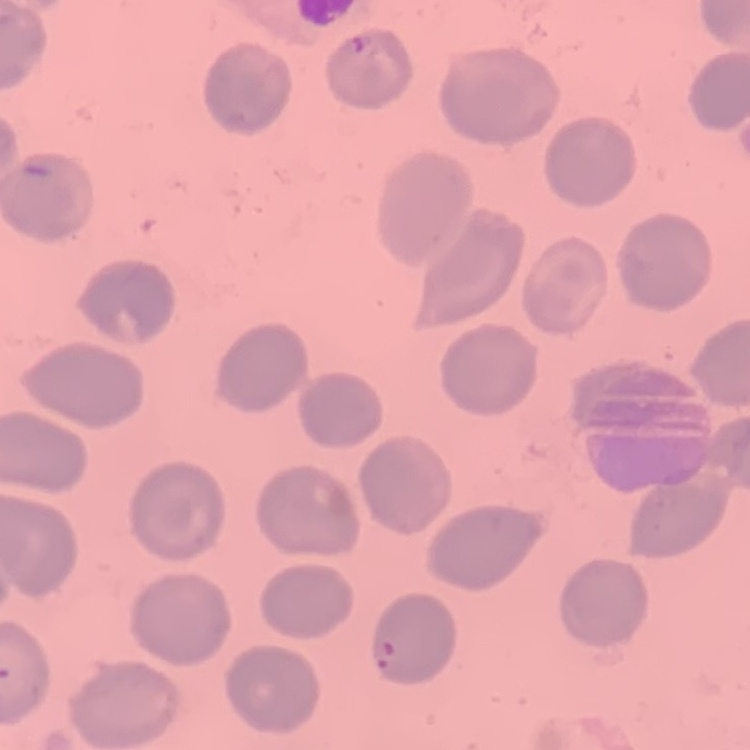

erythrocyte morphology = no rouleaux formation
stain = Field's or Giemsa
preparation = thin blood smear
image type = one tile cut from a larger photomicrograph